Locate and identify every blood parasite.
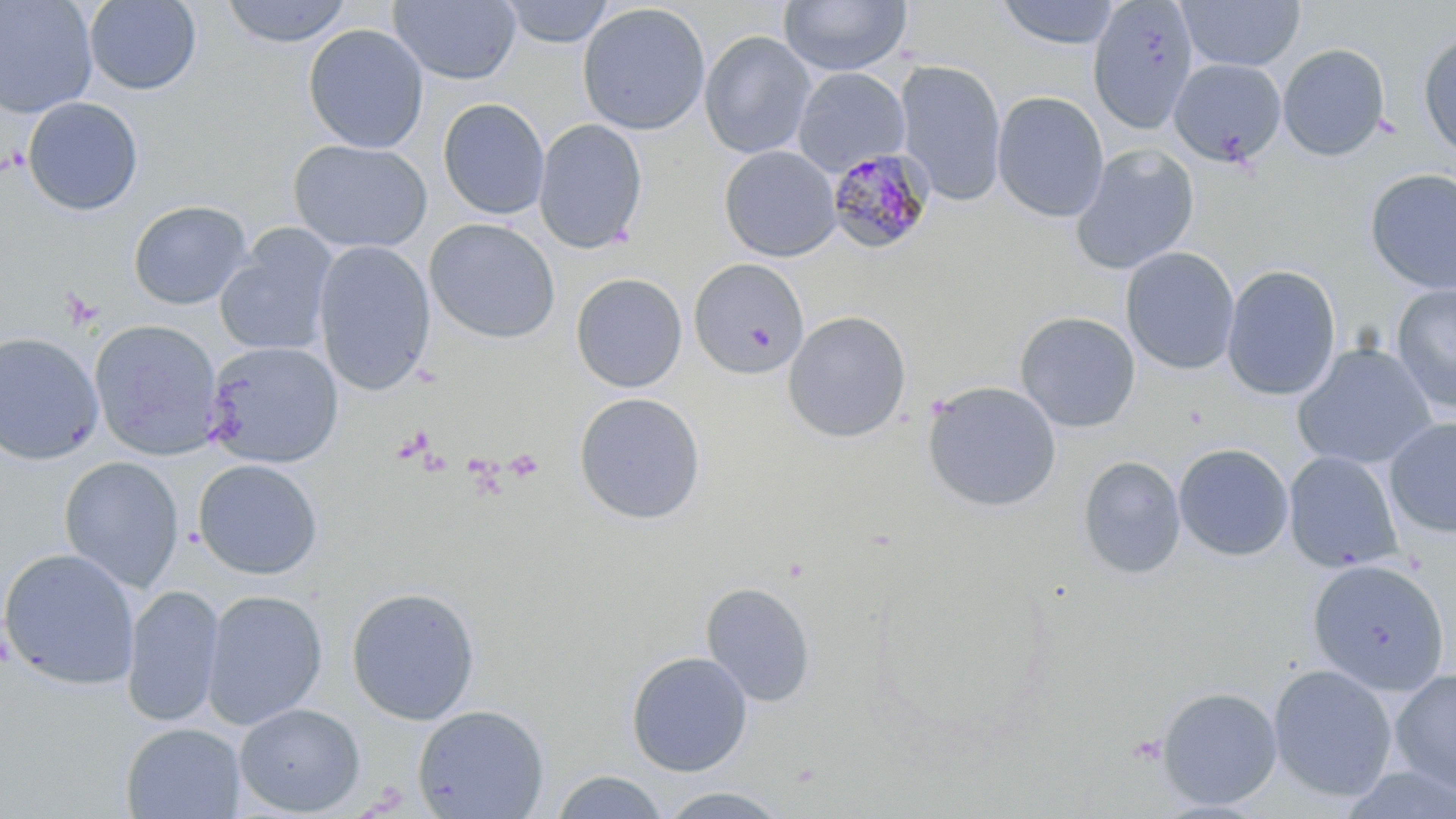

Approximate bounding boxes as (x1, y1, x2, y2) in pixels.
Plasmodium malariae-infected red blood cells: (826, 147, 936, 256).
No Plasmodium falciparum, Plasmodium ovale, Plasmodium vivax, Babesia divergens, or Trypanosoma brucei observed.

Summary:
  - Platelet locations: (504, 450, 545, 481)
  - Uninfected red blood cell locations: (0, 0, 98, 119), (83, 0, 202, 95), (218, 0, 354, 47), (387, 0, 522, 85), (499, 0, 615, 48), (779, 0, 911, 76), (995, 0, 1123, 50), (1087, 0, 1199, 135), (1176, 0, 1305, 72), (576, 2, 711, 136), (302, 23, 429, 154), (1416, 29, 1456, 162), (699, 30, 817, 159), (1278, 44, 1390, 161), (1168, 58, 1287, 168), (894, 59, 1007, 206), (793, 67, 910, 176), (992, 91, 1109, 222), (23, 97, 144, 216), (438, 98, 550, 220), (533, 118, 648, 254), (288, 139, 431, 253), (1070, 143, 1199, 276), (719, 145, 841, 262), (1364, 168, 1456, 295), (128, 200, 252, 310), (424, 218, 561, 344), (213, 225, 338, 357), (313, 240, 435, 396), (1121, 246, 1240, 375), (688, 259, 810, 380), (1221, 264, 1341, 401), (570, 273, 688, 394), (1392, 284, 1456, 415), (783, 310, 912, 443), (1015, 312, 1140, 433), (89, 319, 224, 461), (0, 331, 104, 465), (204, 340, 343, 469), (1292, 342, 1437, 470), (921, 381, 1063, 513), (573, 391, 707, 525), (1383, 416, 1456, 539), (1173, 442, 1294, 561), (1283, 451, 1403, 573), (1077, 455, 1186, 579), (59, 456, 185, 593), (192, 459, 323, 580), (0, 546, 141, 690), (1306, 559, 1450, 696), (700, 582, 816, 707), (121, 583, 225, 727), (346, 585, 481, 725), (202, 589, 328, 730), (625, 650, 753, 776), (1267, 664, 1398, 802), (1389, 668, 1456, 797), (1155, 686, 1283, 810), (234, 703, 366, 815), (412, 704, 550, 818), (120, 722, 246, 819), (1336, 765, 1456, 819), (550, 770, 671, 819), (654, 787, 794, 818)
  - Slide-level diagnosis: Plasmodium malariae
  - Modality: light microscopy
  - Preparation: thin blood film
  - Stain: May-Grünwald-Giemsa
  - Image size: 1456×819 pixels
  - Field of view: one of a larger specimen
  - Magnification: 1000x